State the preparation type.
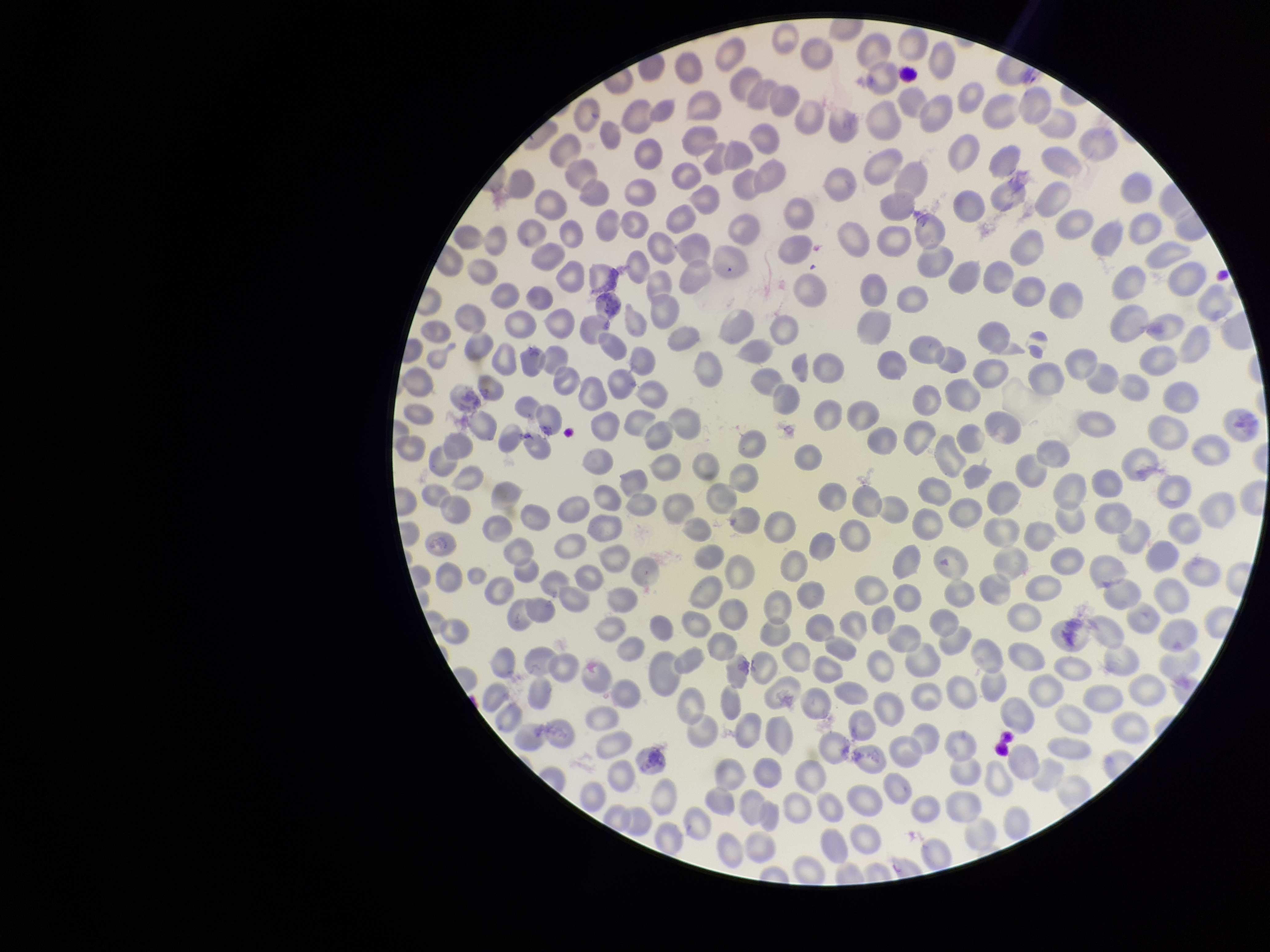

It is a thin blood smear.

Summary:
  - Image size: 1270×952 pixels
  - Red blood cell count: 312
  - Parasitized red blood cells: none detected
  - Parasitized red blood cell count: 0
  - Species reported for this patient: Plasmodium falciparum
  - Stain: Giemsa
  - Patient malaria status: infected
  - Field of view: one from this slide
  - Capture: smartphone photograph through the microscope eyepiece